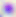 Captured at 400x magnification. Toxoplasma gondii is shown. Photomicrograph.